Assess this cell for malaria.
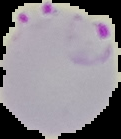

It is parasitized.

Summary:
  - Image type: segmented cell region on a black background
  - Preparation: thin blood smear
  - Image size: 121×139 pixels